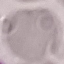

Malaria status: uninfected. Photographed with a smartphone camera at the microscope eyepiece. Giemsa stain. Cell patch, automatically extracted from a larger field of view and resized to 64 × 64 pixels. Thin blood film.